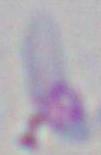

Summary:
  - Magnification: 1000x
  - Identification: Toxoplasma gondii
  - Modality: micrograph